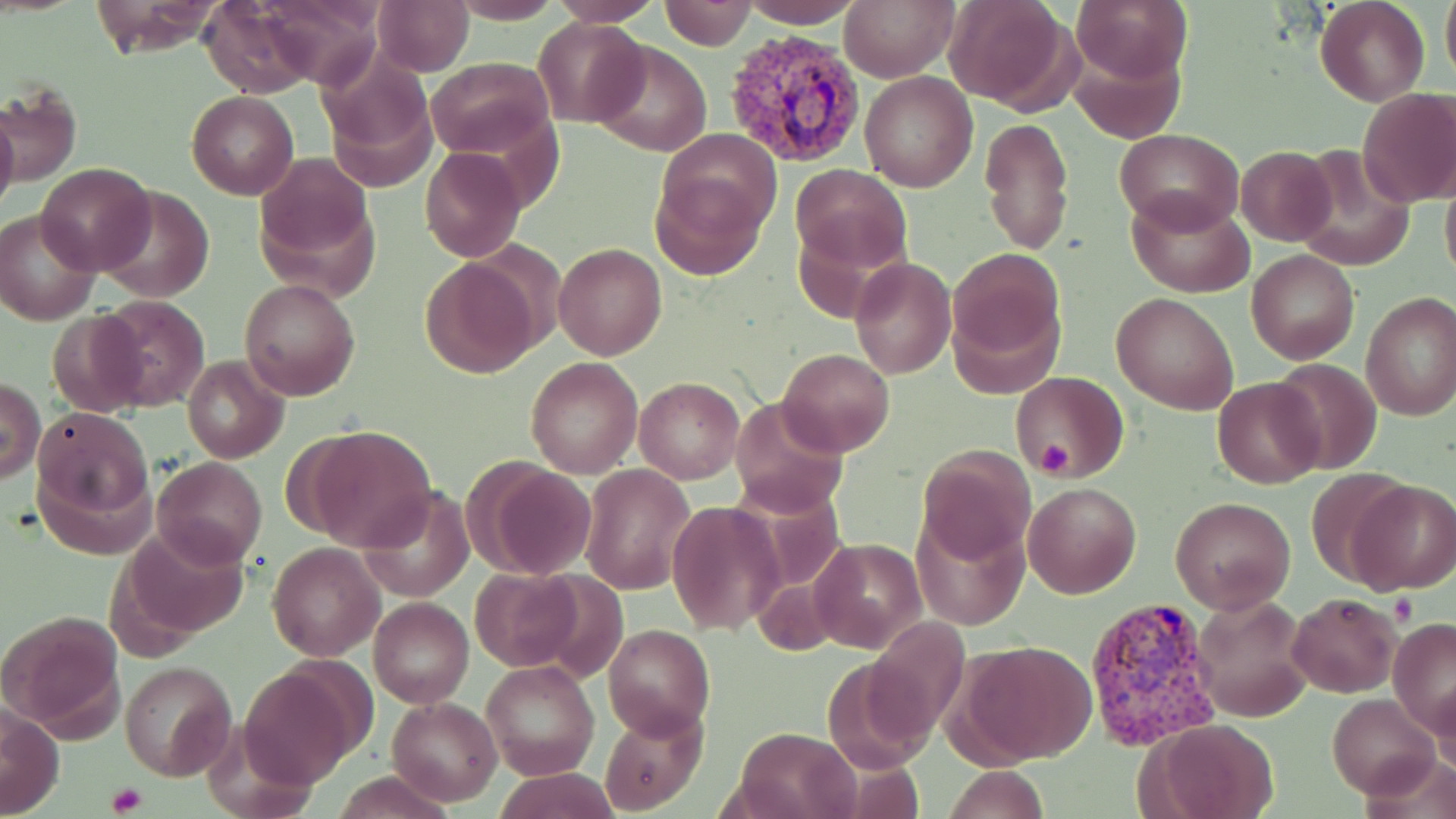

Summary:
  - Coordinate format: approximate bounding boxes as [x1, y1, x2, y2] in pixels
  - Platelet locations: [1036, 440, 1074, 474], [1389, 593, 1419, 625], [106, 782, 147, 814]
  - Uninfected red blood cell locations: [197, 0, 320, 98], [251, 0, 387, 84], [447, 0, 567, 24], [661, 0, 755, 50], [838, 0, 958, 82], [1072, 0, 1193, 86], [1315, 0, 1430, 106], [1441, 0, 1456, 93], [372, 1, 474, 75], [549, 1, 666, 26], [740, 1, 866, 26], [945, 1, 1077, 109], [1336, 8, 1441, 175], [534, 18, 645, 126], [589, 39, 711, 157], [1066, 41, 1186, 146], [317, 45, 441, 186], [427, 57, 555, 159], [859, 71, 978, 192], [1, 83, 80, 189], [1355, 88, 1456, 207], [186, 91, 299, 199], [0, 103, 20, 223], [980, 116, 1074, 256], [657, 128, 783, 237], [1116, 128, 1241, 231], [1236, 146, 1336, 245], [1296, 146, 1415, 270], [420, 147, 526, 263], [253, 151, 377, 277], [35, 163, 155, 275], [792, 164, 910, 274], [651, 170, 765, 277], [1441, 174, 1456, 291], [96, 184, 214, 302], [1126, 191, 1254, 297], [0, 208, 102, 325], [554, 243, 668, 362], [950, 248, 1063, 361], [1246, 249, 1359, 364], [420, 256, 542, 378], [849, 256, 957, 378], [238, 278, 360, 402], [1111, 292, 1238, 413], [1360, 292, 1456, 423], [93, 294, 211, 412], [46, 310, 149, 415], [776, 349, 894, 457], [182, 356, 287, 462], [526, 357, 642, 478], [1269, 358, 1383, 474], [1012, 371, 1125, 478], [1212, 375, 1327, 489], [633, 377, 742, 483], [1, 380, 46, 484], [729, 395, 848, 517], [33, 407, 152, 519], [302, 425, 437, 552], [914, 444, 1034, 562], [153, 456, 267, 567], [472, 461, 599, 579], [582, 464, 696, 594], [1305, 469, 1410, 586], [1351, 481, 1456, 594], [1024, 482, 1142, 599], [361, 484, 474, 602], [1170, 496, 1296, 614], [665, 502, 784, 634], [909, 513, 1029, 630], [122, 524, 249, 644], [810, 538, 926, 653], [268, 542, 384, 662], [470, 567, 585, 671], [1190, 591, 1314, 722], [1287, 593, 1399, 697], [371, 597, 474, 707], [2, 608, 126, 738], [1388, 618, 1456, 732], [603, 624, 714, 739], [961, 640, 1096, 765], [480, 659, 601, 782], [118, 660, 237, 781], [238, 668, 362, 784], [1430, 679, 1456, 781], [1328, 692, 1440, 799], [386, 696, 502, 806], [2, 704, 65, 819], [600, 709, 706, 815], [1145, 717, 1281, 819], [735, 727, 860, 819], [943, 766, 1050, 818], [492, 768, 619, 819], [331, 771, 452, 818]
  - Plasmodium vivax-infected red blood cell locations: [719, 26, 869, 168], [1082, 599, 1226, 748]
  - Slide-level diagnosis: Plasmodium vivax
  - Image size: 1456×819 pixels
  - Preparation: thin blood film
  - Magnification: 1000x
  - Stain: May-Grünwald-Giemsa
  - Modality: optical microscopy
  - Field of view: single